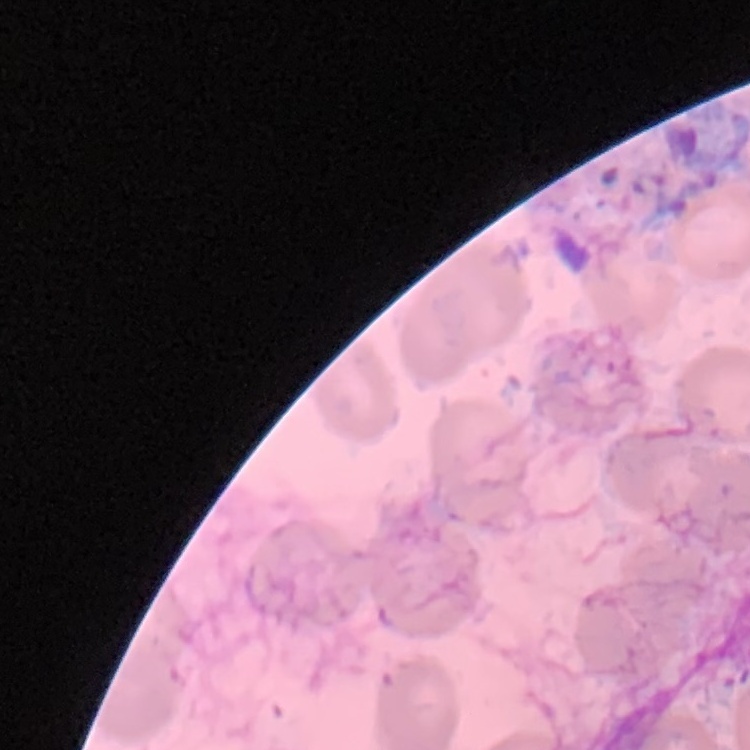

erythrocyte_morphology: no rouleaux formation
stain: Field's or Giemsa
preparation: thin peripheral smear
image_type: one tile cut from a larger photomicrograph